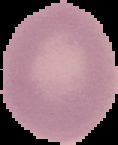

Image is 118×145 pixels. From a thin blood smear. The area outside the segmented cell region is set to black. Malaria status: uninfected.